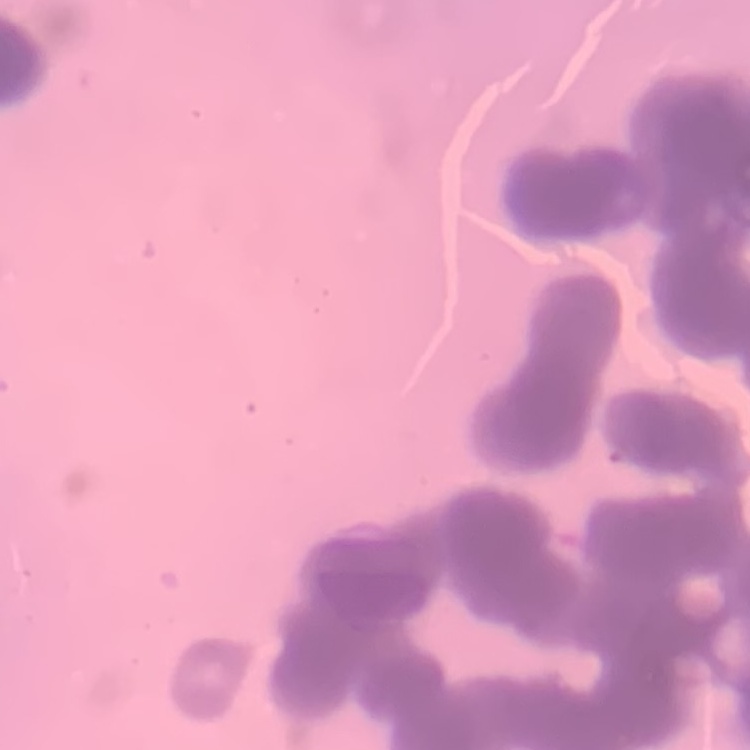

Summary:
  - Erythrocyte morphology: rouleaux formation
  - Image type: square crop of a larger photomicrograph
  - Preparation: thin peripheral smear
  - Stain: Field's or Giemsa